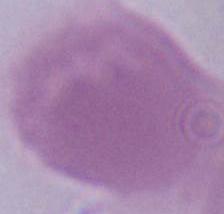
1000x magnification. An erythrocyte is seen. Micrograph.